Name the parasite shown.
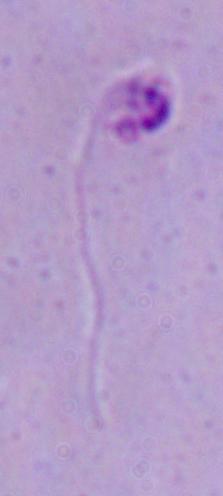

This is Leishmania.

1000x magnification. Micrograph.